Classify this cell by malaria status.
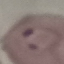
Parasitized.

Summary:
  - Image type: automatically extracted cell patch, resized to 64 × 64 pixels
  - Preparation: thin blood smear
  - Stain: Giemsa
  - Capture: smartphone through the microscope eyepiece